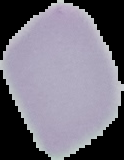

{
  "preparation": "thin blood smear",
  "image_type": "segmented cell region with the area outside set to black",
  "result": "negative for Plasmodium parasites",
  "image_size": "124×160 pixels"
}